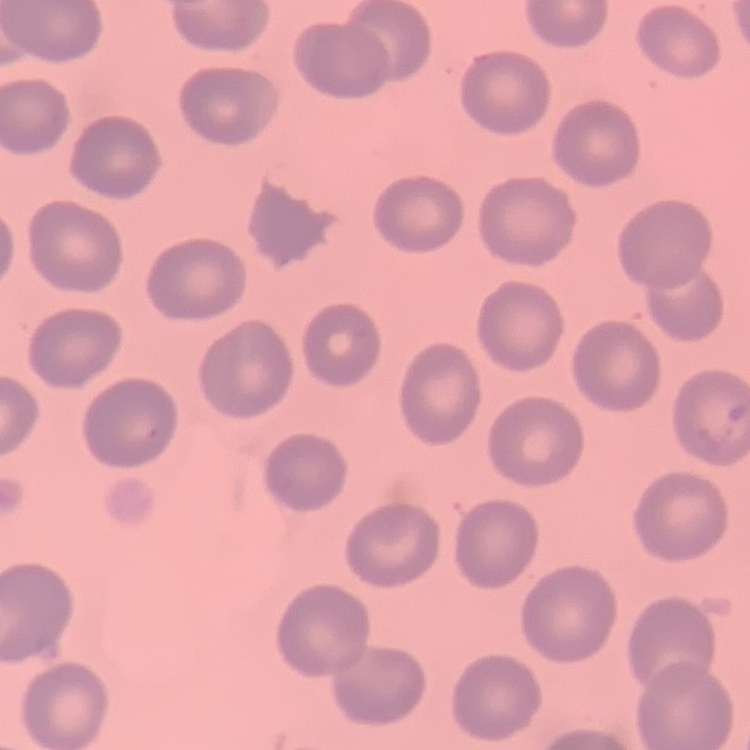 The red blood cells exhibit no rouleaux formation. Thin blood film. One tile cut from a larger photomicrograph. Field's or Giemsa stain.